Assess this cell for malaria.
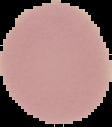

It is uninfected.

image_type: segmented cell region with the area outside set to black
preparation: thin blood smear
image_size: 112×127 pixels